Locate every uninfected red blood cell.
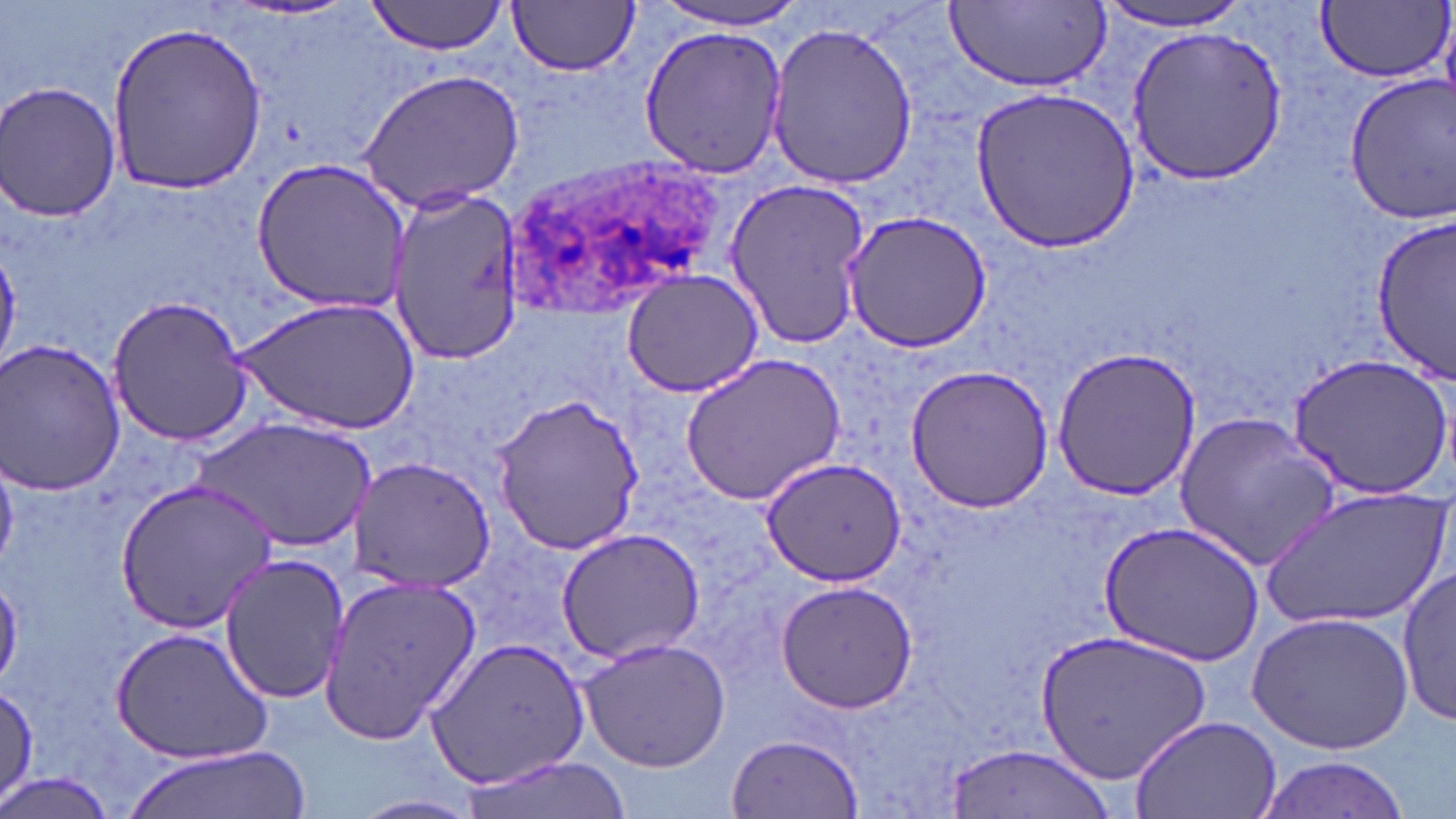
Approximate bounding boxes as [x1, y1, x2, y2] in pixels.
Uninfected red blood cells: [365, 0, 512, 57], [652, 0, 813, 30], [508, 1, 641, 76], [945, 2, 1111, 89], [1317, 2, 1450, 83], [1096, 3, 1259, 34], [107, 17, 268, 193], [766, 20, 919, 190], [639, 24, 787, 178], [1123, 24, 1288, 185], [356, 69, 526, 213], [1342, 71, 1455, 225], [2, 82, 121, 222], [971, 87, 1139, 251], [249, 158, 412, 313], [724, 178, 872, 350], [390, 188, 520, 368], [841, 209, 994, 352], [1373, 214, 1456, 380], [621, 270, 766, 398], [107, 295, 256, 448], [233, 296, 421, 436], [0, 338, 128, 496], [1050, 343, 1201, 502], [678, 351, 848, 507], [1287, 352, 1453, 500], [903, 364, 1057, 514], [491, 393, 646, 556], [1173, 412, 1340, 571], [196, 418, 374, 552], [348, 454, 495, 593], [761, 457, 906, 589], [114, 477, 277, 632], [1264, 482, 1448, 630], [1099, 520, 1264, 666], [554, 527, 707, 664], [219, 553, 349, 705], [1398, 567, 1454, 728], [318, 573, 481, 746], [774, 580, 918, 714], [1248, 611, 1414, 754], [111, 626, 274, 763], [1037, 628, 1212, 788], [425, 635, 589, 790], [579, 637, 730, 772], [1, 681, 39, 806], [1128, 714, 1282, 818], [727, 733, 863, 818], [124, 744, 309, 819], [945, 744, 1113, 818], [1255, 754, 1411, 818], [456, 757, 630, 819], [0, 771, 118, 819], [350, 794, 483, 819].

Summary:
  - Plasmodium ovale-infected red blood cell locations: [501, 156, 732, 315]
  - Slide-level diagnosis: Plasmodium ovale
  - Preparation: thin blood film
  - Image size: 1456×819 pixels
  - Modality: optical microscopy
  - Magnification: 1000x
  - Field of view: one of a larger specimen
  - Stain: May-Grünwald-Giemsa